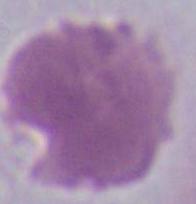

{
  "modality": "photomicrograph",
  "magnification": "1000x",
  "identification": "erythrocyte"
}